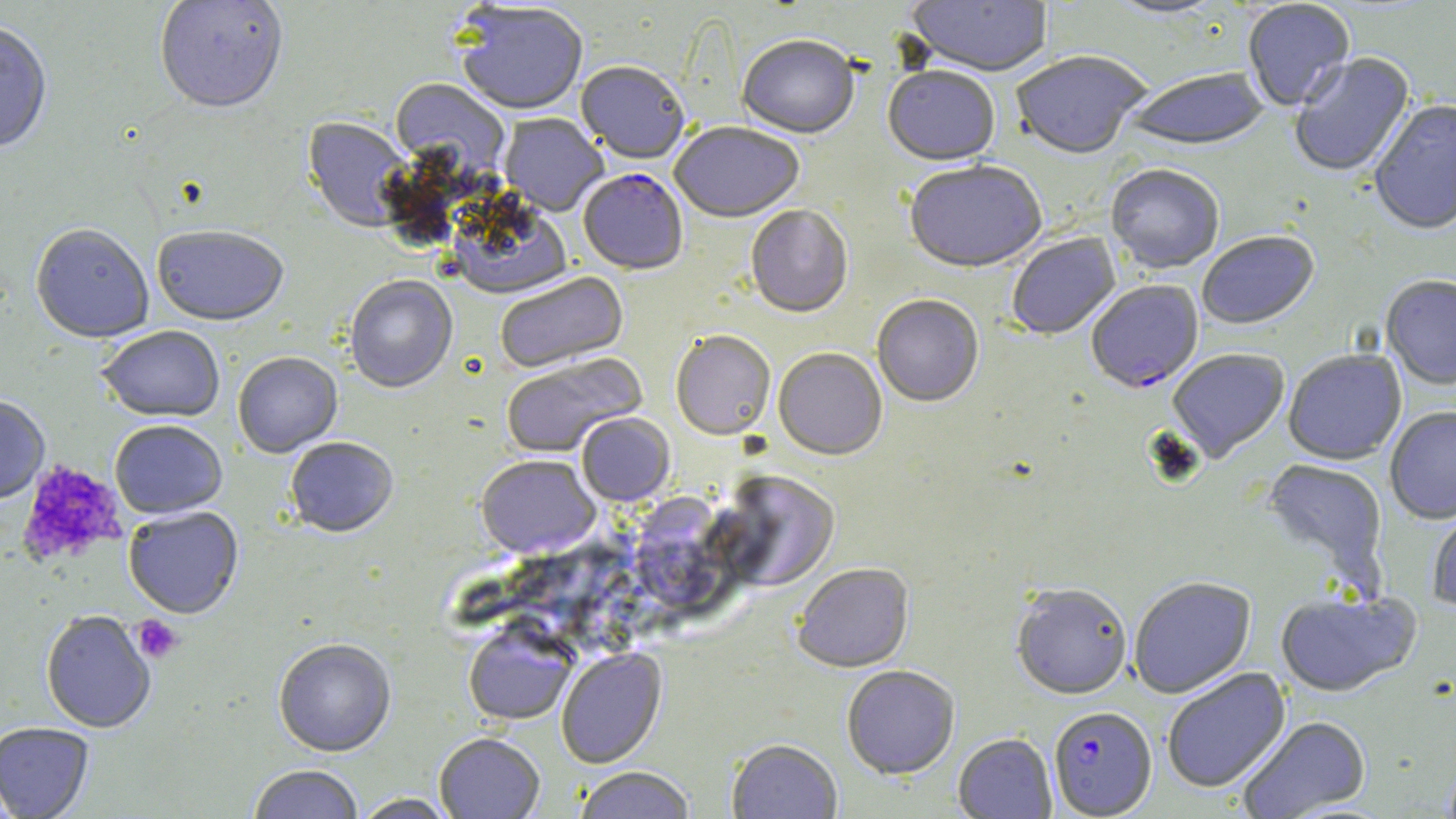
slide-level diagnosis = Plasmodium falciparum
uninfected red blood cell locations (subset) = approximate bounding boxes as (x1,y1)-(x2,y2) corner pairs in pixels: (154,0)-(289,117), (906,0)-(1053,80), (1102,0)-(1230,21), (1242,1)-(1356,113), (454,4)-(588,117), (0,23)-(53,155), (737,38)-(859,140), (1011,53)-(1151,162), (1290,53)-(1416,179), (575,63)-(689,166), (883,69)-(1000,169), (1125,69)-(1269,154), (390,80)-(509,177), (1369,100)-(1456,237), (499,114)-(609,217), (302,118)-(413,234), (669,123)-(804,225), (904,163)-(1047,276), (1106,167)-(1223,275), (450,200)-(573,301), (746,206)-(854,320), (30,226)-(154,345), (151,228)-(289,329), (1198,233)-(1320,332), (1007,234)-(1121,342), (495,272)-(629,375), (1380,276)-(1456,392), (345,277)-(458,395), (871,296)-(984,409), (97,327)-(225,424), (671,332)-(776,442), (1168,349)-(1290,463), (773,350)-(887,462), (1284,350)-(1406,466), (501,353)-(648,459), (233,354)-(342,459), (0,397)-(50,505), (1386,408)-(1456,525), (576,415)-(675,506), (110,421)-(227,520), (285,439)-(398,540), (476,456)-(600,560), (1261,459)-(1388,588), (711,471)-(841,594), (637,484)-(732,621), (1427,504)-(1456,613), (124,508)-(243,620), (792,564)-(915,675), (1129,578)-(1256,700), (1011,586)-(1132,702), (1276,591)-(1421,700), (41,611)-(155,733), (463,621)-(577,727), (273,640)-(397,759), (556,648)-(668,770), (842,667)-(959,780), (1163,668)-(1291,794), (1236,717)-(1372,819), (0,723)-(94,819), (953,734)-(1057,818), (434,735)-(545,818), (727,741)-(843,818), (249,766)-(364,819), (574,768)-(695,819), (352,794)-(458,819)
field of view = one of a larger specimen
image size = 1456×819 pixels
magnification = 1000x
platelet locations = approximate bounding boxes as (x1,y1)-(x2,y2) corner pairs in pixels: (16,460)-(126,567), (132,616)-(183,664)
Plasmodium falciparum-infected red blood cell locations (subset) = approximate bounding boxes as (x1,y1)-(x2,y2) corner pairs in pixels: (1086,282)-(1203,396), (1049,707)-(1157,818)
stain = May-Grünwald-Giemsa
modality = light microscopy
preparation = thin blood smear